Describe the morphology of the red blood cells.
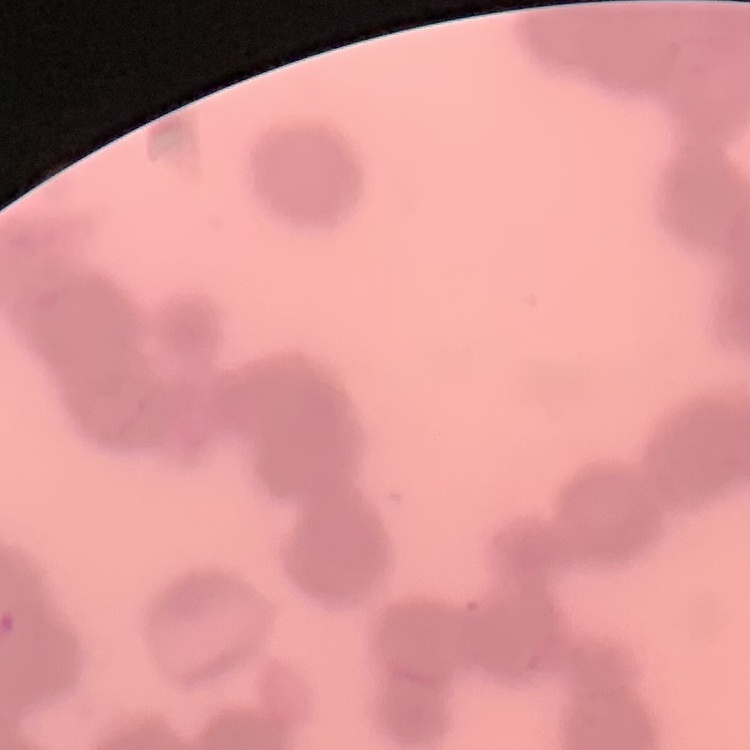
They show rouleaux formation.

{
  "preparation": "thin blood smear",
  "stain": "Field's or Giemsa",
  "image_type": "square crop of a larger photomicrograph"
}